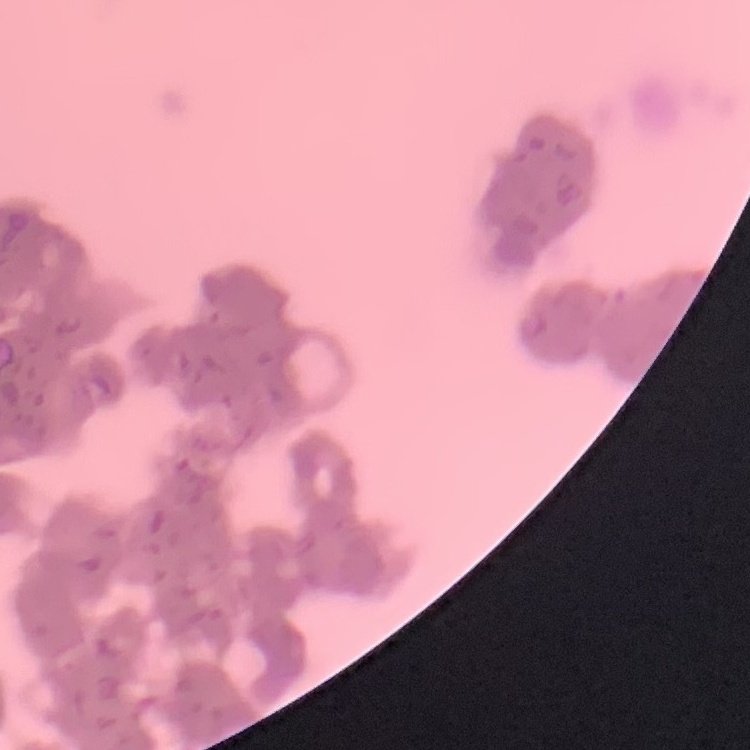

{
  "red_blood_cell_morphology": "rouleaux formation",
  "preparation": "thin blood film",
  "image_type": "one tile cut from a larger photomicrograph",
  "stain": "Field's or Giemsa"
}